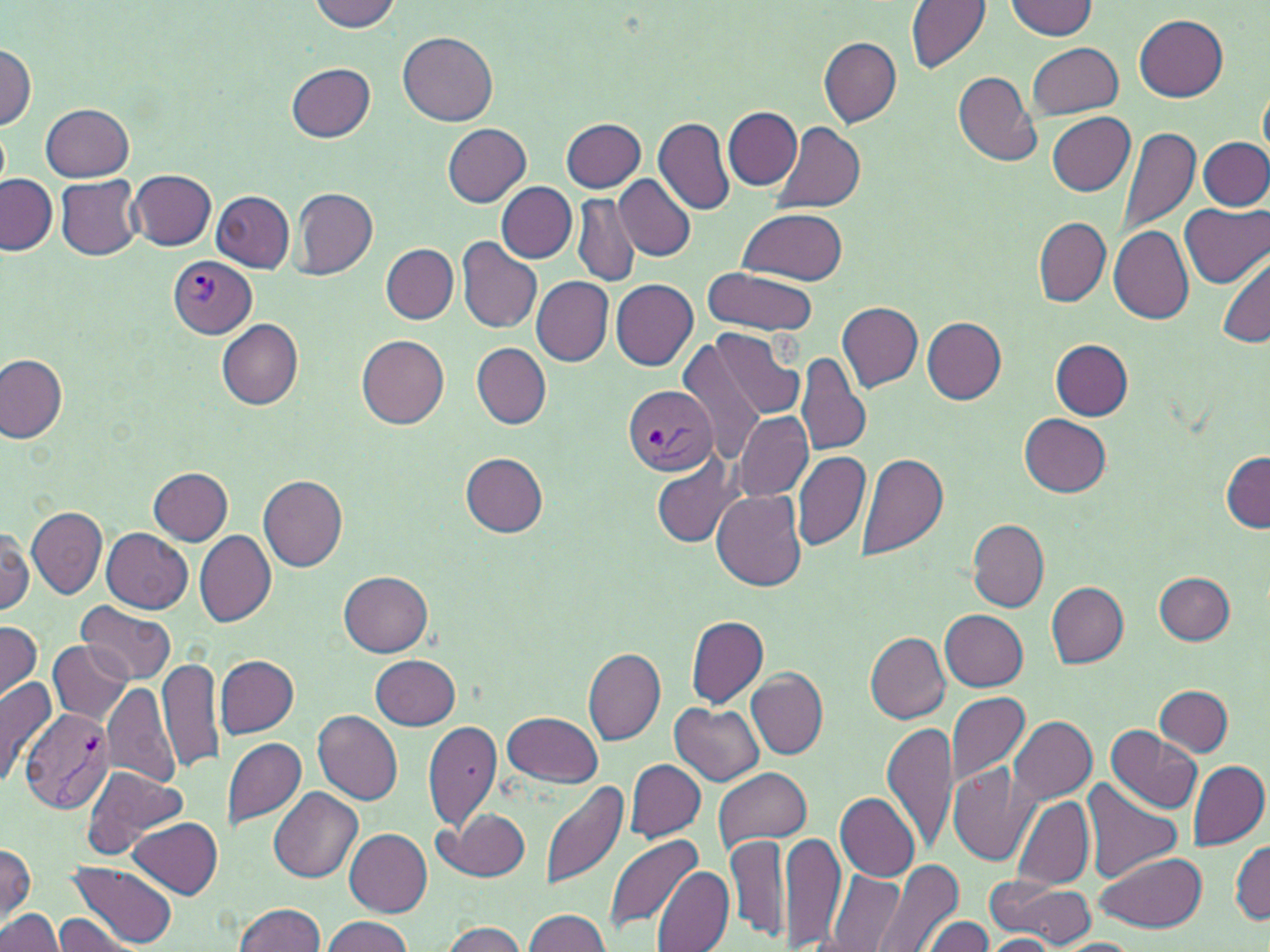
Approximate bounding boxes as named x1/y1/x2/y2 corners in pixels. Plasmodium vivax-infected red blood cell locations: (x1=168, y1=256, x2=255, y2=338), (x1=624, y1=385, x2=718, y2=475), (x1=19, y1=707, x2=116, y2=814). Uninfected red blood cell locations: (x1=307, y1=0, x2=402, y2=32), (x1=907, y1=0, x2=991, y2=71), (x1=1006, y1=1, x2=1098, y2=39), (x1=1133, y1=13, x2=1227, y2=102), (x1=398, y1=32, x2=498, y2=126), (x1=820, y1=38, x2=902, y2=127), (x1=1, y1=40, x2=35, y2=130), (x1=1027, y1=41, x2=1123, y2=118), (x1=287, y1=63, x2=375, y2=141), (x1=952, y1=70, x2=1040, y2=166), (x1=1259, y1=83, x2=1269, y2=164), (x1=41, y1=103, x2=133, y2=181), (x1=724, y1=107, x2=802, y2=188), (x1=1047, y1=111, x2=1135, y2=195), (x1=654, y1=116, x2=734, y2=216), (x1=561, y1=118, x2=645, y2=191), (x1=773, y1=121, x2=866, y2=214), (x1=443, y1=124, x2=530, y2=207), (x1=1118, y1=126, x2=1200, y2=237), (x1=1200, y1=138, x2=1270, y2=210), (x1=128, y1=169, x2=216, y2=250), (x1=0, y1=174, x2=57, y2=255), (x1=614, y1=174, x2=696, y2=261), (x1=56, y1=175, x2=143, y2=261), (x1=497, y1=183, x2=577, y2=263), (x1=293, y1=187, x2=377, y2=279), (x1=210, y1=191, x2=294, y2=273), (x1=572, y1=194, x2=640, y2=288), (x1=1181, y1=201, x2=1270, y2=288), (x1=737, y1=206, x2=847, y2=286), (x1=1034, y1=218, x2=1110, y2=305), (x1=1108, y1=227, x2=1193, y2=324), (x1=456, y1=237, x2=543, y2=334), (x1=381, y1=243, x2=457, y2=323), (x1=1217, y1=256, x2=1270, y2=348), (x1=701, y1=266, x2=820, y2=337), (x1=532, y1=276, x2=612, y2=365), (x1=611, y1=279, x2=699, y2=371), (x1=836, y1=299, x2=923, y2=392), (x1=216, y1=317, x2=302, y2=409), (x1=922, y1=317, x2=1007, y2=404), (x1=710, y1=328, x2=805, y2=422), (x1=357, y1=335, x2=450, y2=429), (x1=1050, y1=338, x2=1133, y2=419), (x1=677, y1=340, x2=766, y2=464), (x1=472, y1=343, x2=552, y2=428), (x1=797, y1=351, x2=872, y2=459), (x1=0, y1=354, x2=67, y2=442), (x1=733, y1=410, x2=812, y2=501), (x1=1020, y1=414, x2=1112, y2=496), (x1=1220, y1=451, x2=1270, y2=532), (x1=792, y1=452, x2=869, y2=551), (x1=461, y1=453, x2=547, y2=537), (x1=856, y1=453, x2=949, y2=562), (x1=650, y1=456, x2=742, y2=548), (x1=149, y1=467, x2=233, y2=545), (x1=258, y1=475, x2=347, y2=571), (x1=712, y1=489, x2=806, y2=591), (x1=27, y1=505, x2=107, y2=598), (x1=969, y1=518, x2=1049, y2=611), (x1=0, y1=527, x2=32, y2=617), (x1=102, y1=527, x2=194, y2=611), (x1=194, y1=529, x2=276, y2=627), (x1=339, y1=571, x2=432, y2=656), (x1=1155, y1=571, x2=1234, y2=645), (x1=1046, y1=582, x2=1128, y2=668), (x1=75, y1=601, x2=177, y2=683), (x1=941, y1=610, x2=1028, y2=690), (x1=686, y1=616, x2=768, y2=709), (x1=0, y1=621, x2=43, y2=704), (x1=867, y1=632, x2=949, y2=723), (x1=49, y1=641, x2=131, y2=724), (x1=582, y1=646, x2=666, y2=745), (x1=371, y1=654, x2=461, y2=730), (x1=216, y1=655, x2=299, y2=737), (x1=158, y1=656, x2=226, y2=775), (x1=745, y1=669, x2=827, y2=759), (x1=0, y1=675, x2=56, y2=789), (x1=676, y1=681, x2=831, y2=770), (x1=101, y1=683, x2=181, y2=786), (x1=1155, y1=686, x2=1233, y2=757), (x1=944, y1=690, x2=1030, y2=789), (x1=671, y1=704, x2=763, y2=785), (x1=312, y1=709, x2=403, y2=805), (x1=503, y1=710, x2=603, y2=787), (x1=1008, y1=714, x2=1097, y2=804), (x1=424, y1=715, x2=503, y2=835), (x1=883, y1=718, x2=957, y2=855), (x1=1104, y1=725, x2=1201, y2=815), (x1=222, y1=736, x2=306, y2=829), (x1=624, y1=759, x2=705, y2=839), (x1=947, y1=759, x2=1041, y2=870), (x1=1186, y1=759, x2=1268, y2=852), (x1=81, y1=765, x2=185, y2=858), (x1=713, y1=766, x2=812, y2=850), (x1=541, y1=779, x2=628, y2=892), (x1=1081, y1=779, x2=1185, y2=883), (x1=267, y1=787, x2=362, y2=883), (x1=835, y1=793, x2=921, y2=881), (x1=1011, y1=795, x2=1094, y2=890), (x1=437, y1=808, x2=531, y2=881), (x1=129, y1=817, x2=222, y2=897), (x1=343, y1=827, x2=431, y2=916), (x1=781, y1=831, x2=845, y2=948), (x1=604, y1=832, x2=703, y2=934), (x1=727, y1=832, x2=790, y2=943), (x1=1232, y1=839, x2=1269, y2=925), (x1=0, y1=844, x2=35, y2=925), (x1=1096, y1=852, x2=1206, y2=933), (x1=871, y1=860, x2=964, y2=952), (x1=67, y1=863, x2=178, y2=948), (x1=652, y1=866, x2=733, y2=952), (x1=827, y1=870, x2=905, y2=950), (x1=985, y1=877, x2=1097, y2=946), (x1=233, y1=901, x2=325, y2=952), (x1=0, y1=909, x2=64, y2=952), (x1=523, y1=909, x2=610, y2=952), (x1=53, y1=915, x2=141, y2=950), (x1=320, y1=916, x2=413, y2=952), (x1=923, y1=916, x2=995, y2=952), (x1=440, y1=921, x2=531, y2=952), (x1=982, y1=934, x2=1060, y2=950), (x1=1056, y1=937, x2=1141, y2=952). Platelet locations: (x1=766, y1=322, x2=809, y2=370). Slide-level diagnosis: Plasmodium vivax. Light microscopy. Thin blood smear. Image is 1270×952 pixels. Captured at 1000x magnification. May-Grünwald-Giemsa-stained preparation. One field of a larger specimen.